Assess this cell for malaria.
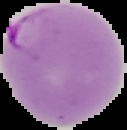

Parasitized.

Image is 127×130 pixels. From a thin blood smear. Segmented cell region on a black background.